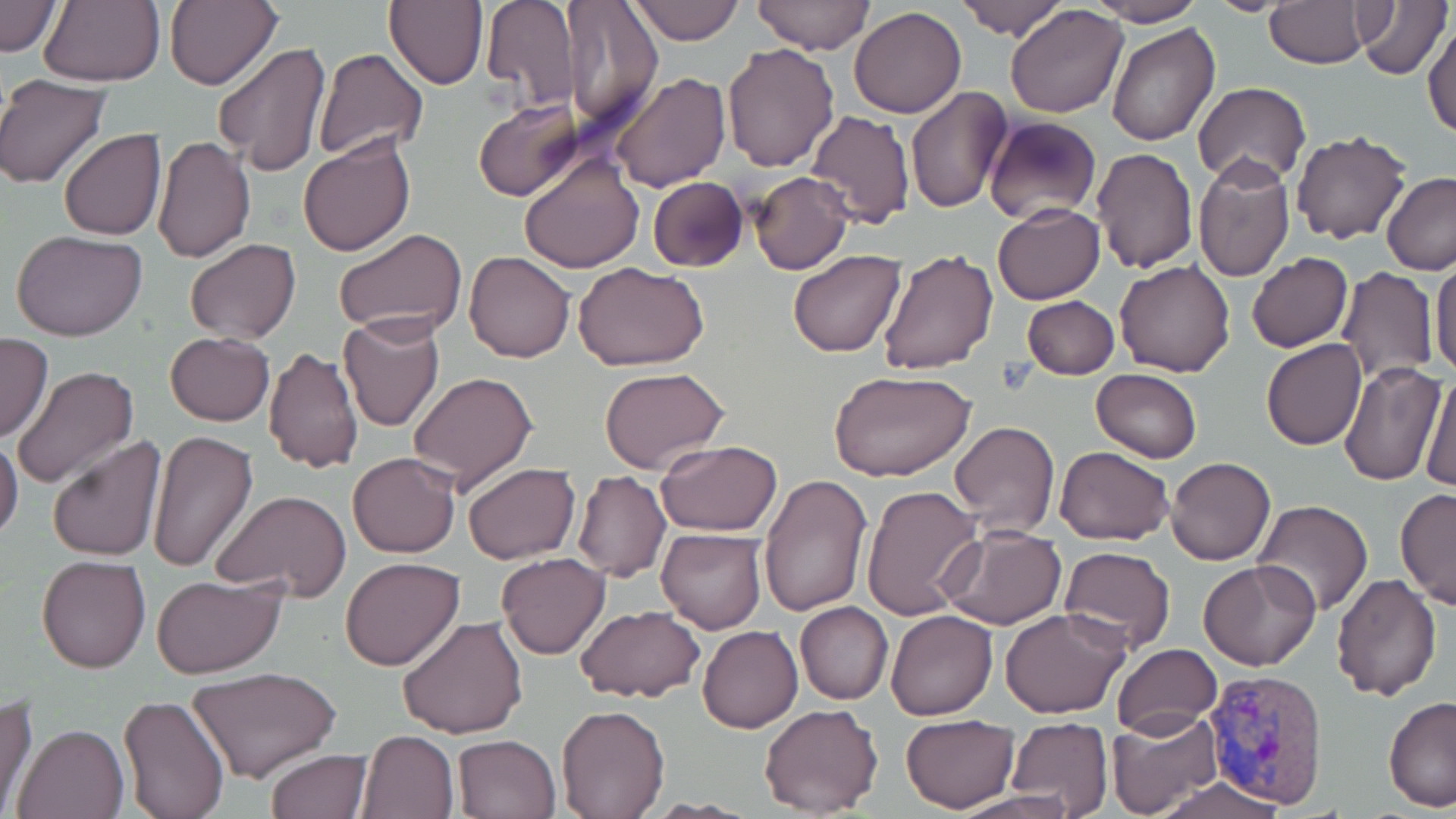

Approximate bounding boxes as [x1, y1, x2, y2] in pixels. Plasmodium vivax-infected red blood cell locations: [1200, 668, 1330, 810]. Uninfected red blood cell locations: [0, 0, 64, 57], [38, 0, 165, 86], [165, 0, 282, 91], [385, 0, 487, 89], [629, 0, 746, 45], [751, 0, 873, 55], [958, 0, 1067, 41], [1087, 0, 1207, 26], [1204, 0, 1299, 17], [1356, 0, 1451, 81], [480, 1, 578, 110], [1265, 2, 1371, 69], [561, 3, 663, 131], [1004, 4, 1128, 118], [847, 6, 966, 118], [1422, 16, 1456, 140], [1107, 23, 1219, 147], [213, 42, 332, 178], [720, 43, 840, 174], [311, 48, 428, 162], [609, 71, 730, 193], [0, 75, 111, 189], [1193, 82, 1311, 185], [904, 84, 1013, 214], [475, 99, 584, 201], [804, 109, 916, 228], [984, 116, 1100, 223], [45, 126, 160, 338], [1290, 129, 1412, 245], [59, 130, 167, 242], [297, 133, 416, 259], [151, 134, 257, 262], [1090, 147, 1199, 275], [519, 154, 644, 273], [1193, 156, 1294, 283], [750, 171, 853, 275], [1381, 172, 1456, 274], [646, 176, 748, 272], [992, 202, 1105, 304], [334, 228, 467, 340], [11, 231, 150, 343], [184, 239, 301, 344], [878, 246, 1001, 376], [463, 250, 575, 363], [788, 250, 905, 358], [1246, 252, 1353, 353], [1431, 256, 1456, 380], [1114, 259, 1236, 377], [573, 262, 710, 371], [1338, 268, 1438, 382], [1022, 294, 1120, 379], [337, 314, 446, 434], [166, 331, 273, 425], [0, 334, 54, 443], [1261, 339, 1367, 449], [265, 346, 363, 474], [1339, 361, 1446, 485], [12, 365, 139, 490], [599, 366, 729, 476], [828, 366, 978, 482], [1090, 367, 1202, 462], [407, 369, 539, 495], [1420, 369, 1456, 494], [949, 420, 1060, 538], [145, 429, 259, 574], [905, 430, 1034, 594], [0, 434, 23, 544], [47, 434, 167, 561], [657, 440, 783, 537], [1054, 446, 1175, 544], [348, 453, 460, 558], [1165, 456, 1275, 566], [461, 463, 580, 564], [573, 471, 671, 582], [568, 473, 672, 699], [756, 473, 872, 617], [859, 482, 985, 620], [1396, 488, 1456, 611], [210, 491, 352, 603], [1254, 499, 1375, 616], [939, 524, 1067, 631], [656, 528, 768, 633], [1059, 545, 1176, 653], [496, 552, 610, 659], [36, 554, 150, 673], [340, 557, 465, 671], [1198, 559, 1323, 672], [1331, 571, 1442, 701], [150, 576, 286, 678], [355, 578, 501, 717], [795, 602, 893, 704], [574, 604, 705, 703], [999, 607, 1130, 718], [885, 610, 997, 720], [397, 615, 530, 740], [697, 625, 803, 733], [1111, 644, 1223, 737], [187, 665, 342, 784], [0, 693, 40, 815], [1383, 694, 1456, 813], [117, 695, 230, 819], [555, 704, 670, 818], [759, 704, 885, 818], [1106, 708, 1224, 819], [900, 713, 1019, 813], [1005, 716, 1114, 816], [12, 723, 127, 819], [356, 729, 459, 819], [453, 734, 560, 818], [264, 747, 373, 818], [1146, 774, 1289, 819], [943, 792, 1083, 819]. Slide-level diagnosis: Plasmodium vivax. May-Grünwald-Giemsa stain. Image is 1456×819 pixels. Thin blood smear. Light microscopy. One field of a larger specimen. 1000x magnification.